Identify the cell.
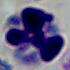
A leukocyte.

Micrograph. Captured at 1000x magnification.